Outline platelets.
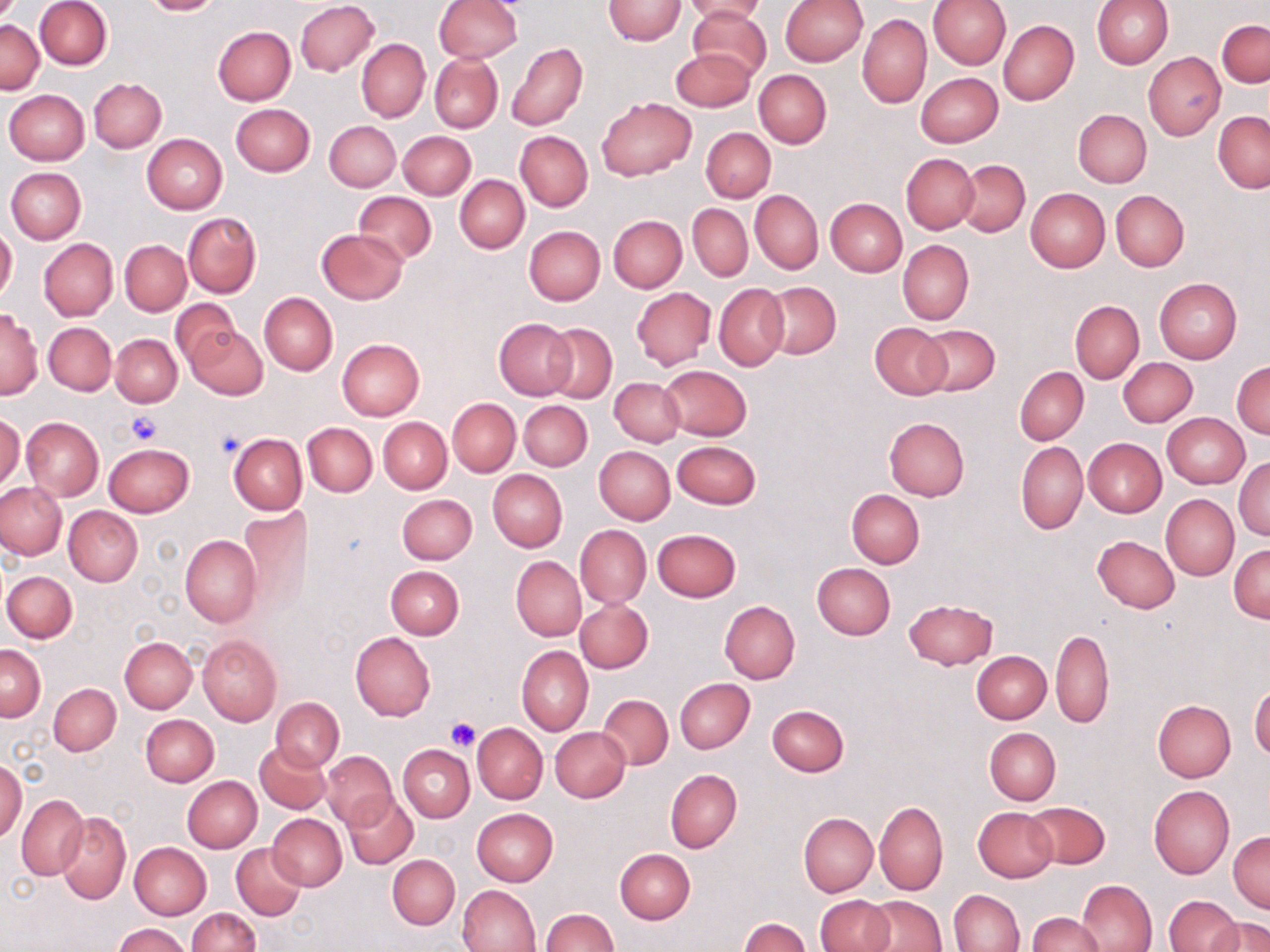
Approximate bounding boxes as named x1/y1/x2/y2 corners in pixels.
Platelets: (x1=126, y1=412, x2=163, y2=445), (x1=215, y1=427, x2=247, y2=460), (x1=445, y1=716, x2=481, y2=752).

Uninfected red blood cell locations: (x1=35, y1=0, x2=112, y2=70), (x1=140, y1=0, x2=225, y2=16), (x1=434, y1=0, x2=522, y2=62), (x1=603, y1=0, x2=685, y2=45), (x1=682, y1=0, x2=768, y2=23), (x1=780, y1=0, x2=867, y2=67), (x1=929, y1=0, x2=1011, y2=70), (x1=1091, y1=0, x2=1173, y2=69), (x1=295, y1=1, x2=379, y2=76), (x1=689, y1=8, x2=771, y2=81), (x1=858, y1=14, x2=931, y2=107), (x1=1, y1=19, x2=44, y2=93), (x1=1218, y1=19, x2=1269, y2=88), (x1=998, y1=20, x2=1079, y2=104), (x1=212, y1=26, x2=296, y2=105), (x1=356, y1=39, x2=430, y2=122), (x1=506, y1=42, x2=588, y2=131), (x1=671, y1=48, x2=756, y2=112), (x1=1144, y1=52, x2=1225, y2=139), (x1=430, y1=54, x2=503, y2=132), (x1=754, y1=70, x2=831, y2=147), (x1=916, y1=72, x2=1003, y2=147), (x1=89, y1=78, x2=166, y2=152), (x1=4, y1=89, x2=90, y2=164), (x1=596, y1=98, x2=696, y2=180), (x1=231, y1=103, x2=315, y2=176), (x1=1073, y1=109, x2=1152, y2=187), (x1=1212, y1=111, x2=1269, y2=192), (x1=325, y1=120, x2=399, y2=190), (x1=701, y1=126, x2=775, y2=202), (x1=399, y1=130, x2=476, y2=199), (x1=515, y1=131, x2=593, y2=211), (x1=142, y1=134, x2=228, y2=214), (x1=901, y1=153, x2=979, y2=232), (x1=956, y1=160, x2=1031, y2=237), (x1=5, y1=167, x2=86, y2=244), (x1=456, y1=175, x2=528, y2=253), (x1=1025, y1=187, x2=1110, y2=272), (x1=750, y1=190, x2=823, y2=274), (x1=1111, y1=190, x2=1190, y2=272), (x1=354, y1=192, x2=436, y2=265), (x1=825, y1=198, x2=907, y2=277), (x1=688, y1=204, x2=752, y2=281), (x1=183, y1=212, x2=260, y2=296), (x1=609, y1=215, x2=686, y2=292), (x1=0, y1=226, x2=17, y2=302), (x1=524, y1=226, x2=605, y2=305), (x1=317, y1=228, x2=407, y2=304), (x1=38, y1=238, x2=118, y2=321), (x1=120, y1=240, x2=191, y2=315), (x1=897, y1=240, x2=973, y2=325), (x1=1154, y1=277, x2=1242, y2=365), (x1=763, y1=282, x2=841, y2=358), (x1=715, y1=283, x2=789, y2=371), (x1=630, y1=287, x2=715, y2=369), (x1=259, y1=292, x2=337, y2=375), (x1=172, y1=299, x2=238, y2=371), (x1=1070, y1=301, x2=1144, y2=383), (x1=1, y1=310, x2=42, y2=400), (x1=494, y1=318, x2=576, y2=399), (x1=44, y1=322, x2=116, y2=395), (x1=544, y1=322, x2=617, y2=403), (x1=869, y1=322, x2=951, y2=399), (x1=186, y1=324, x2=268, y2=400), (x1=918, y1=325, x2=1000, y2=397), (x1=111, y1=334, x2=182, y2=407), (x1=336, y1=338, x2=425, y2=420), (x1=1118, y1=357, x2=1197, y2=427), (x1=1231, y1=361, x2=1270, y2=439), (x1=659, y1=365, x2=752, y2=440), (x1=1015, y1=366, x2=1088, y2=444), (x1=610, y1=377, x2=685, y2=446), (x1=447, y1=398, x2=520, y2=476), (x1=519, y1=400, x2=592, y2=471), (x1=1163, y1=412, x2=1250, y2=488), (x1=0, y1=414, x2=24, y2=491), (x1=21, y1=416, x2=104, y2=501), (x1=379, y1=417, x2=452, y2=493), (x1=884, y1=417, x2=969, y2=501), (x1=303, y1=422, x2=377, y2=496), (x1=228, y1=432, x2=307, y2=514), (x1=1083, y1=438, x2=1166, y2=516), (x1=674, y1=440, x2=761, y2=508), (x1=1016, y1=441, x2=1087, y2=533), (x1=103, y1=443, x2=194, y2=518), (x1=594, y1=446, x2=675, y2=525), (x1=1234, y1=456, x2=1270, y2=541), (x1=488, y1=469, x2=567, y2=553), (x1=0, y1=481, x2=66, y2=559), (x1=846, y1=490, x2=924, y2=568), (x1=397, y1=493, x2=477, y2=564), (x1=1161, y1=495, x2=1239, y2=579), (x1=394, y1=496, x2=470, y2=641), (x1=238, y1=504, x2=311, y2=612), (x1=64, y1=505, x2=143, y2=586), (x1=575, y1=524, x2=650, y2=608), (x1=651, y1=528, x2=742, y2=602), (x1=179, y1=535, x2=261, y2=627), (x1=1091, y1=535, x2=1179, y2=613), (x1=1229, y1=543, x2=1270, y2=622), (x1=511, y1=556, x2=586, y2=640), (x1=812, y1=563, x2=894, y2=639), (x1=386, y1=565, x2=463, y2=638), (x1=3, y1=570, x2=76, y2=642), (x1=902, y1=598, x2=998, y2=669), (x1=576, y1=599, x2=653, y2=673), (x1=719, y1=600, x2=800, y2=684), (x1=1050, y1=628, x2=1114, y2=729), (x1=350, y1=632, x2=435, y2=721), (x1=197, y1=635, x2=282, y2=725), (x1=120, y1=637, x2=197, y2=713), (x1=1, y1=645, x2=45, y2=721), (x1=517, y1=646, x2=593, y2=736), (x1=973, y1=651, x2=1050, y2=723), (x1=675, y1=678, x2=755, y2=754), (x1=48, y1=683, x2=121, y2=755), (x1=1249, y1=683, x2=1270, y2=760), (x1=599, y1=694, x2=672, y2=769), (x1=271, y1=697, x2=344, y2=771), (x1=1153, y1=700, x2=1236, y2=781), (x1=766, y1=704, x2=848, y2=777), (x1=140, y1=714, x2=219, y2=786), (x1=474, y1=723, x2=547, y2=804), (x1=550, y1=727, x2=630, y2=801), (x1=985, y1=727, x2=1060, y2=805), (x1=255, y1=741, x2=329, y2=814), (x1=399, y1=745, x2=474, y2=822), (x1=321, y1=751, x2=397, y2=830), (x1=0, y1=759, x2=26, y2=843), (x1=665, y1=769, x2=742, y2=853), (x1=182, y1=776, x2=262, y2=852), (x1=1148, y1=784, x2=1235, y2=879), (x1=342, y1=792, x2=419, y2=868), (x1=17, y1=794, x2=88, y2=880), (x1=875, y1=801, x2=948, y2=895), (x1=1025, y1=801, x2=1110, y2=869), (x1=973, y1=807, x2=1057, y2=882), (x1=471, y1=808, x2=558, y2=886), (x1=798, y1=812, x2=877, y2=896), (x1=56, y1=813, x2=131, y2=903), (x1=266, y1=813, x2=347, y2=890), (x1=1229, y1=830, x2=1270, y2=912), (x1=129, y1=842, x2=211, y2=919), (x1=232, y1=844, x2=307, y2=920), (x1=614, y1=848, x2=695, y2=923), (x1=387, y1=854, x2=459, y2=929), (x1=1076, y1=880, x2=1156, y2=951), (x1=455, y1=884, x2=540, y2=952), (x1=949, y1=889, x2=1024, y2=951), (x1=814, y1=895, x2=894, y2=952), (x1=865, y1=895, x2=945, y2=951), (x1=1164, y1=895, x2=1241, y2=952), (x1=187, y1=907, x2=261, y2=952), (x1=540, y1=909, x2=617, y2=951), (x1=1026, y1=913, x2=1104, y2=952), (x1=1208, y1=916, x2=1269, y2=952), (x1=738, y1=918, x2=810, y2=952), (x1=113, y1=923, x2=192, y2=952). Slide-level diagnosis: no evidence of blood parasites. Image is 1270×952 pixels. Thin blood film. One field of a larger specimen. Light microscopy. 1000x magnification. May-Grünwald-Giemsa-stained preparation.